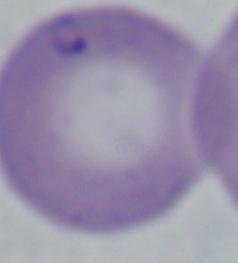
Photomicrograph. 1000x magnification. A Babesia parasite is shown.